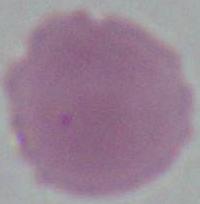

Captured at 1000x magnification. Photomicrograph. An erythrocyte is seen.